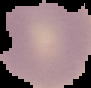

Malaria status: uninfected. Cell region segmented out of the field of view; the surrounding area is masked to black. Image is 91×88 pixels. From a thin blood film.